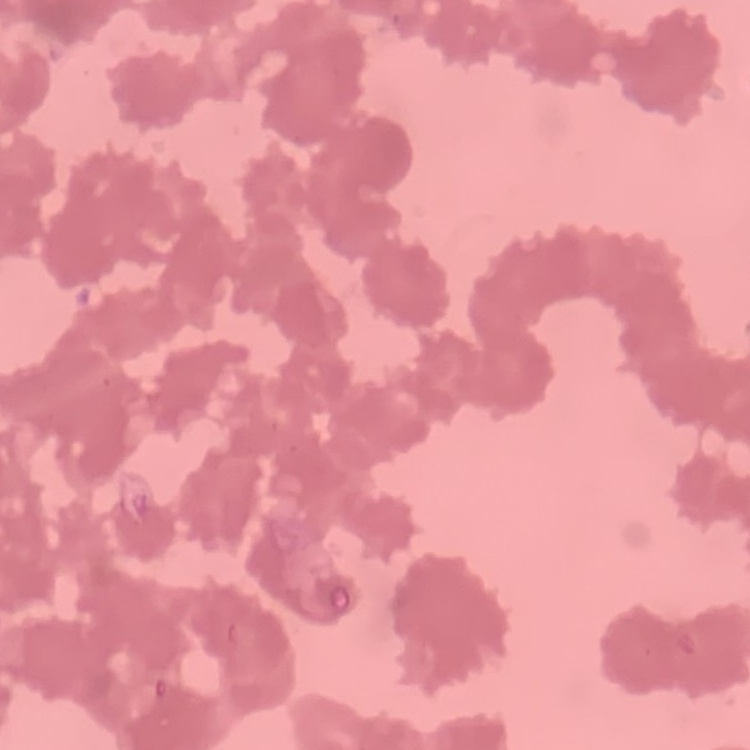
The erythrocytes exhibit rouleaux formation. Thin blood smear. Square crop of a larger photomicrograph. Stained with either Field's or Giemsa.